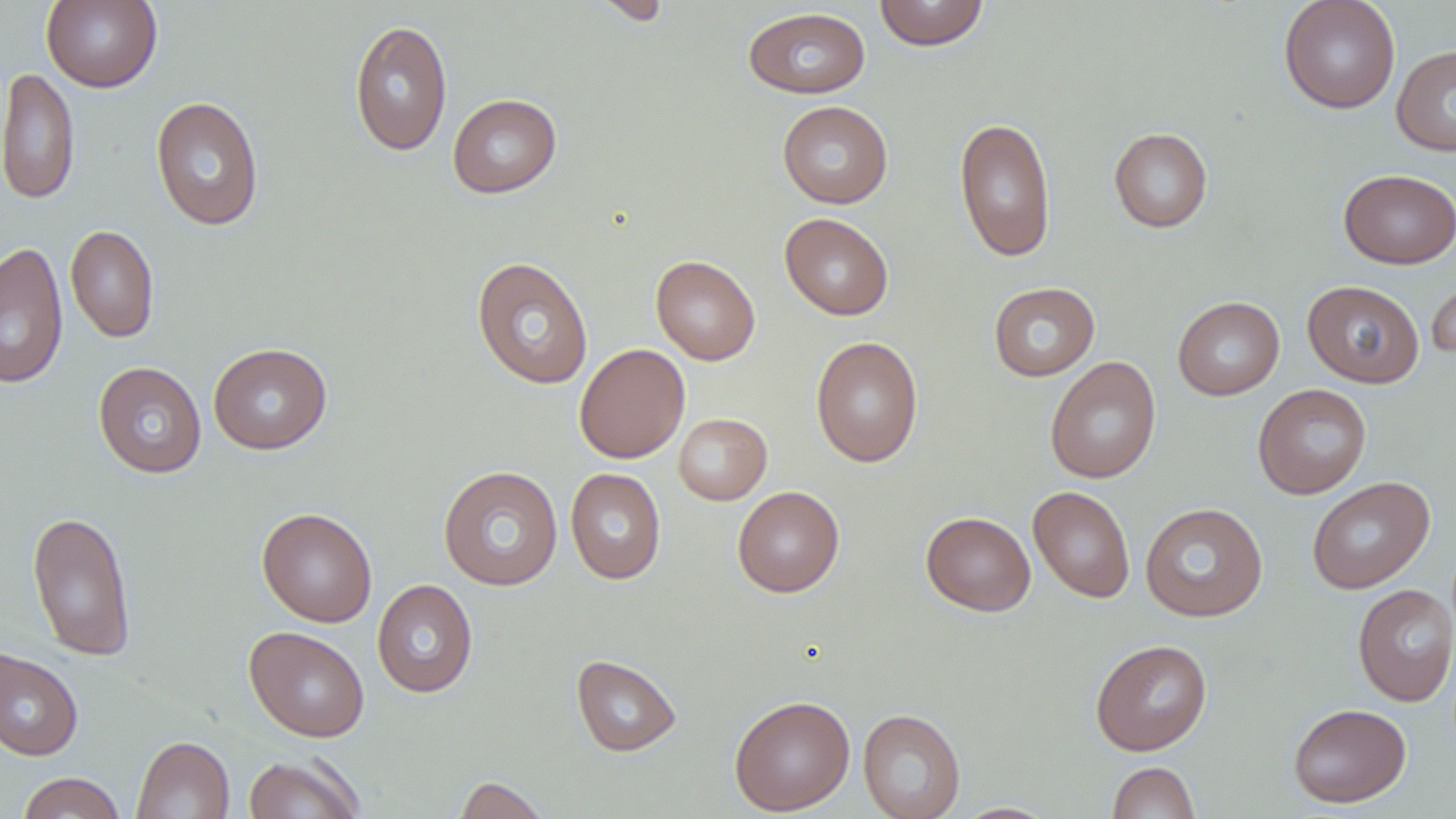
slide_level_diagnosis: negative for blood parasites
magnification: 1000x
preparation: thin blood smear
stain: May-Grünwald-Giemsa
uninfected_red_blood_cell_locations: 'approximate bounding boxes as named x1/y1/x2/y2 corners in pixels: (x1=42, y1=0, x2=162, y2=92), (x1=591, y1=0, x2=672, y2=25), (x1=873, y1=0, x2=990, y2=51), (x1=1278, y1=0, x2=1401, y2=114), (x1=743, y1=7, x2=871, y2=98), (x1=349, y1=19, x2=452, y2=156), (x1=1391, y1=44, x2=1456, y2=157), (x1=0, y1=67, x2=80, y2=205), (x1=447, y1=93, x2=562, y2=198), (x1=150, y1=95, x2=264, y2=231), (x1=777, y1=101, x2=893, y2=208), (x1=954, y1=117, x2=1057, y2=263), (x1=1108, y1=127, x2=1212, y2=232), (x1=1339, y1=168, x2=1456, y2=269), (x1=779, y1=213, x2=894, y2=320), (x1=65, y1=225, x2=160, y2=344), (x1=0, y1=240, x2=69, y2=388), (x1=651, y1=255, x2=760, y2=365), (x1=471, y1=256, x2=593, y2=389), (x1=1426, y1=272, x2=1456, y2=364), (x1=1302, y1=280, x2=1424, y2=388), (x1=987, y1=281, x2=1100, y2=382), (x1=1173, y1=296, x2=1284, y2=400), (x1=810, y1=336, x2=924, y2=468), (x1=208, y1=342, x2=332, y2=454), (x1=574, y1=343, x2=690, y2=463), (x1=1045, y1=356, x2=1161, y2=484), (x1=93, y1=361, x2=207, y2=478), (x1=1252, y1=383, x2=1371, y2=499), (x1=673, y1=413, x2=772, y2=505), (x1=438, y1=465, x2=563, y2=590), (x1=565, y1=467, x2=665, y2=584), (x1=1307, y1=476, x2=1434, y2=594), (x1=732, y1=486, x2=845, y2=597), (x1=1027, y1=486, x2=1136, y2=604), (x1=1140, y1=502, x2=1268, y2=622), (x1=257, y1=507, x2=377, y2=627), (x1=27, y1=509, x2=137, y2=662), (x1=921, y1=511, x2=1035, y2=616), (x1=372, y1=578, x2=478, y2=698), (x1=1352, y1=583, x2=1456, y2=706), (x1=244, y1=626, x2=370, y2=743), (x1=1090, y1=639, x2=1212, y2=756), (x1=0, y1=647, x2=84, y2=761), (x1=571, y1=654, x2=681, y2=756), (x1=729, y1=695, x2=855, y2=815), (x1=1288, y1=702, x2=1411, y2=808), (x1=858, y1=708, x2=965, y2=819), (x1=131, y1=735, x2=235, y2=819), (x1=243, y1=753, x2=366, y2=819), (x1=1107, y1=761, x2=1200, y2=819), (x1=18, y1=772, x2=126, y2=818), (x1=453, y1=776, x2=550, y2=818), (x1=953, y1=802, x2=1058, y2=818)'
image_size: 1456×819 pixels
field_of_view: single
modality: light microscopy